Describe the morphology of the erythrocytes.
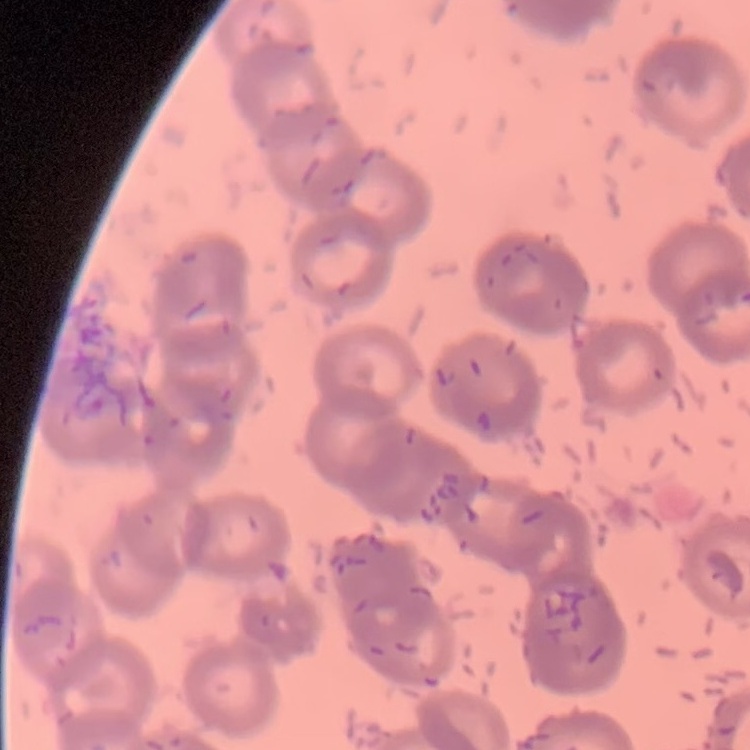

Rouleaux formation.

Thin blood film. One tile cut from a larger photomicrograph. Field's or Giemsa stain.